Assess the morphology of the red blood cells.
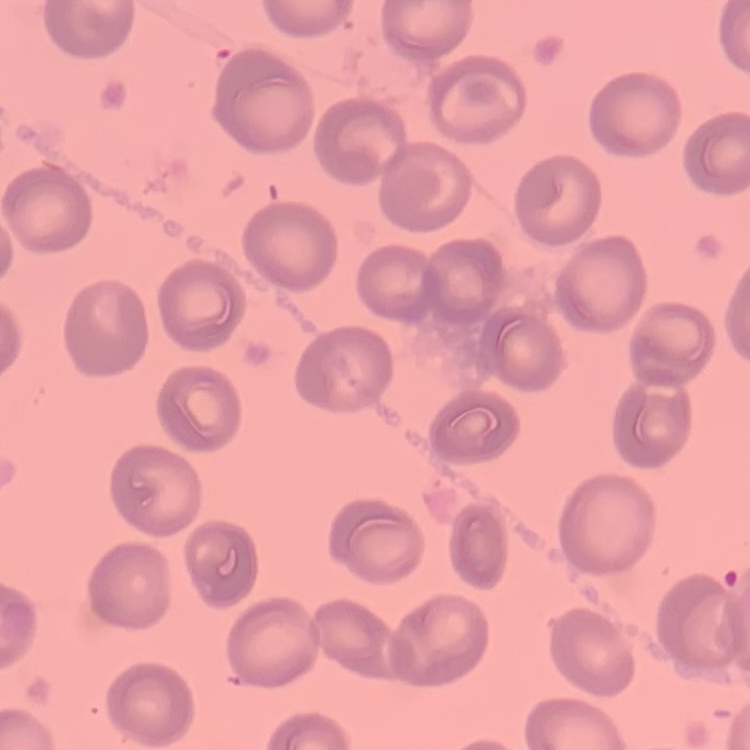
No rouleaux formation.

image_type: square crop of a larger photomicrograph
stain: Field's or Giemsa
preparation: thin blood film